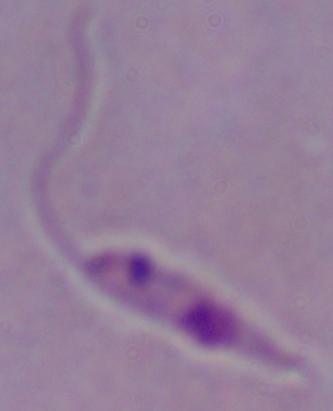
identification = Leishmania
modality = micrograph
magnification = 1000x